Assess this cell for malaria.
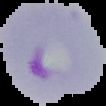
It is parasitized.

preparation = thin blood film
image type = cell region segmented out of the field of view; surrounding area masked to black
image size = 106×106 pixels